State which cell type is depicted.
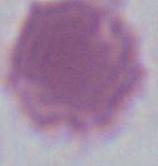
This is an erythrocyte.

magnification: 1000x
modality: micrograph